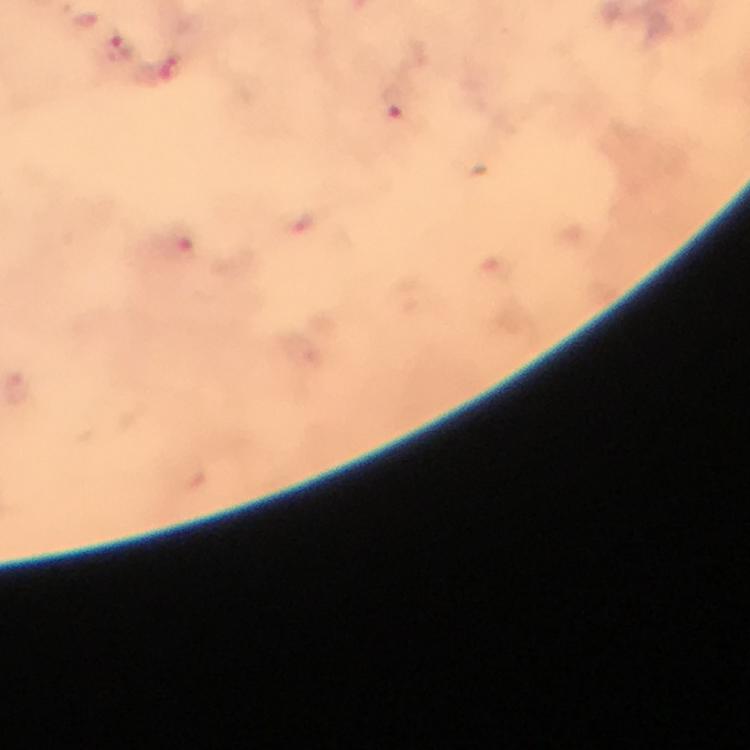
Approximate centers as (x, y) in pixels. Malaria parasite locations: (83, 21), (118, 51), (162, 70), (394, 103), (176, 245). Giemsa stain. From a malaria diagnostic workup. Thick blood smear. A crop from one field of view. 100x magnification. Photographed with a smartphone mounted on the microscope. Immersion oil was used. Image is 750×750 pixels.